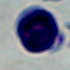

Captured at 1000x magnification. A white blood cell is shown. Photomicrograph.